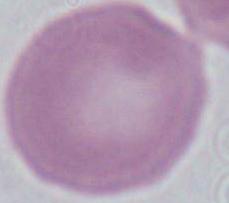 Captured at 1000x magnification. An erythrocyte is shown. Photomicrograph.